Give the position of every malaria parasite and every leukocyte.
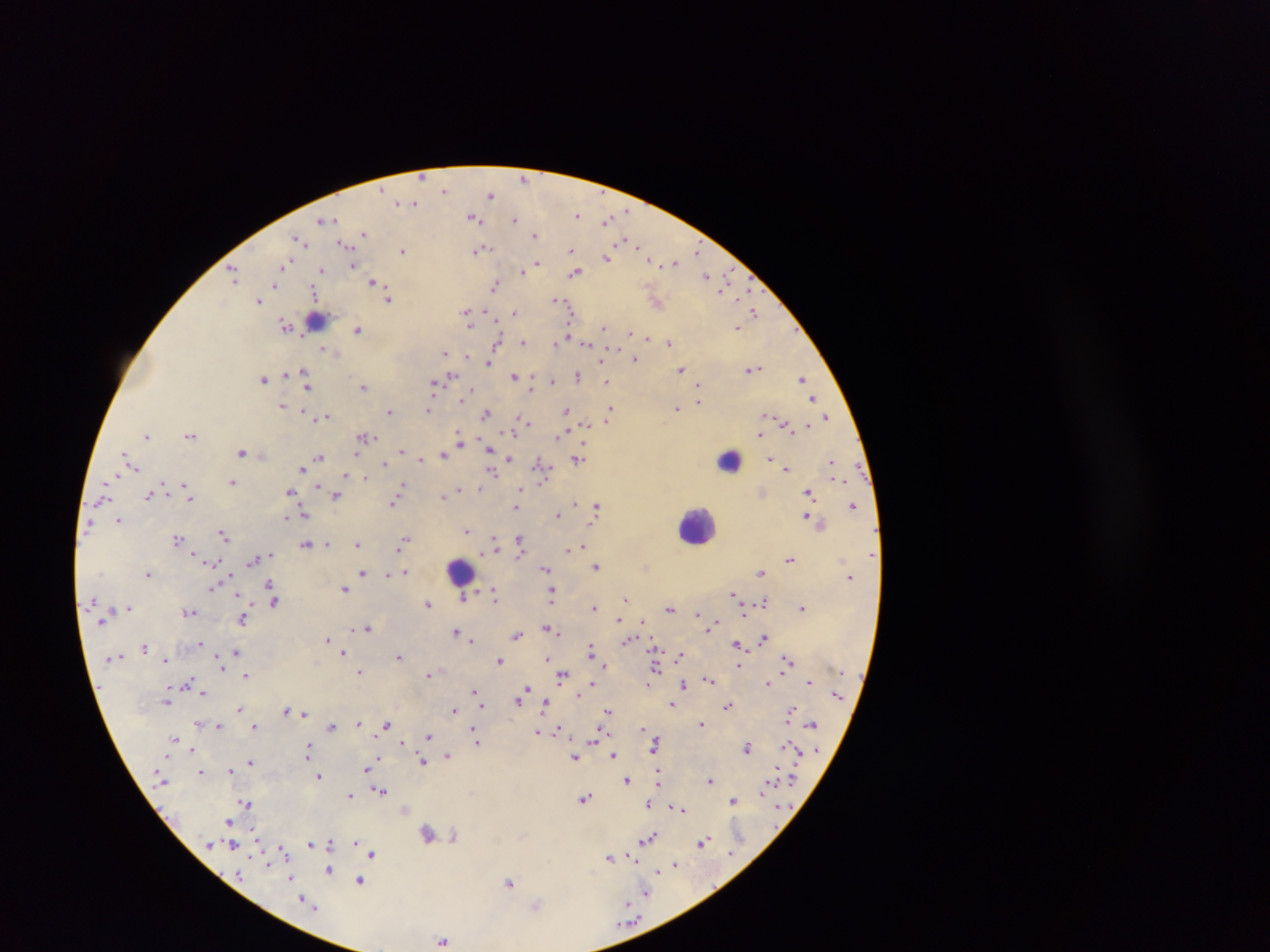
Approximate centers as x y in pixels.
Malaria parasites: 424 178; 523 178; 443 191; 490 193; 415 202; 625 209; 577 215; 475 218; 514 218; 332 219; 607 219; 321 220; 535 232; 362 233; 626 241; 303 242; 341 243; 482 249; 572 250; 402 251; 696 251; 606 258; 286 263; 538 263; 674 264; 353 265; 321 269; 521 271; 575 273; 706 274; 233 276; 371 281; 274 285; 496 286; 313 292; 558 299; 259 300; 389 300; 513 311; 753 311; 466 312; 484 312; 467 319; 286 325; 605 328; 359 330; 568 334; 629 334; 644 337; 565 340; 524 342; 671 342; 496 343; 555 343; 323 348; 446 353; 467 356; 635 360; 487 362; 599 363; 304 368; 681 368; 754 370; 577 374; 514 375; 451 377; 802 377; 264 379; 552 381; 607 383; 433 386; 305 387; 363 387; 472 390; 464 397; 814 399; 701 401; 282 405; 611 408; 678 408; 429 409; 566 410; 307 412; 390 412; 486 414; 518 416; 827 416; 771 417; 327 418; 524 422; 586 423; 786 425; 760 434; 147 436; 189 436; 367 436; 563 437; 459 439; 461 443; 487 448; 401 450; 242 451; 357 452; 442 456; 321 457; 422 458; 771 458; 510 459; 577 460; 384 463; 537 463; 829 463; 786 468; 303 469; 493 471; 345 475; 366 478; 840 478; 233 481; 402 486; 185 487; 319 487; 521 487; 292 492; 808 492; 337 495; 443 495; 147 497; 191 497; 392 503; 576 503; 598 504; 853 505; 515 508; 304 512; 559 515; 807 516; 288 517; 119 519; 467 530; 224 534; 405 537; 177 538; 494 538; 520 539; 358 543; 305 544; 584 545; 494 546; 400 548; 193 551; 566 551; 790 560; 253 562; 215 563; 598 566; 222 569; 545 569; 404 571; 362 573; 762 573; 147 574; 389 574; 268 584; 210 587; 346 589; 479 589; 495 593; 551 593; 238 594; 734 594; 464 597; 626 597; 237 598; 495 599; 274 602; 763 602; 428 604; 129 606; 804 606; 800 607; 593 608; 671 608; 190 613; 697 613; 242 620; 619 620; 642 622; 715 625; 368 627; 543 629; 550 629; 366 630; 708 630; 456 631; 554 632; 459 634; 559 634; 517 637; 764 637; 327 638; 471 642; 203 643; 736 644; 145 646; 653 647; 591 649; 343 652; 235 653; 680 655; 401 657; 546 659; 164 660; 788 660; 500 662; 605 665; 738 666; 223 669; 658 670; 360 671; 428 675; 562 675; 247 676; 190 678; 709 678; 188 681; 807 682; 767 683; 592 684; 685 684; 527 689; 472 692; 576 694; 202 695; 518 701; 545 702; 671 703; 481 705; 727 706; 239 708; 454 709; 607 709; 791 709; 287 710; 304 714; 359 723; 386 724; 703 724; 810 724; 196 725; 219 725; 256 726; 331 726; 558 727; 474 728; 641 729; 537 731; 429 736; 175 738; 593 740; 479 742; 401 744; 790 744; 785 745; 654 746; 308 747; 191 748; 749 749; 306 752; 449 754; 614 754; 378 756; 574 757; 250 763; 422 763; 249 764; 368 768; 230 770; 367 771; 201 772; 320 776; 659 777; 628 782; 710 782; 770 783; 789 783; 766 786; 380 792; 352 795; 585 798; 735 800; 245 803; 648 803; 734 805; 673 808; 685 809; 226 821; 254 831; 427 832; 454 836; 653 836; 650 839; 329 843; 704 843; 310 844; 353 844; 208 845; 281 846; 233 847; 284 850; 729 851; 373 854; 630 854; 610 859; 635 861; 675 863; 329 871; 659 872; 289 877; 359 879; 509 883; 646 893; 300 897; 629 903; 443 939.
No leukocytes observed.

Summary:
  - Country: Ghana
  - Capture: mobile-phone photograph through a microscope
  - Field of view: single
  - Preparation: thick blood smear
  - Image size: 1270×952 pixels